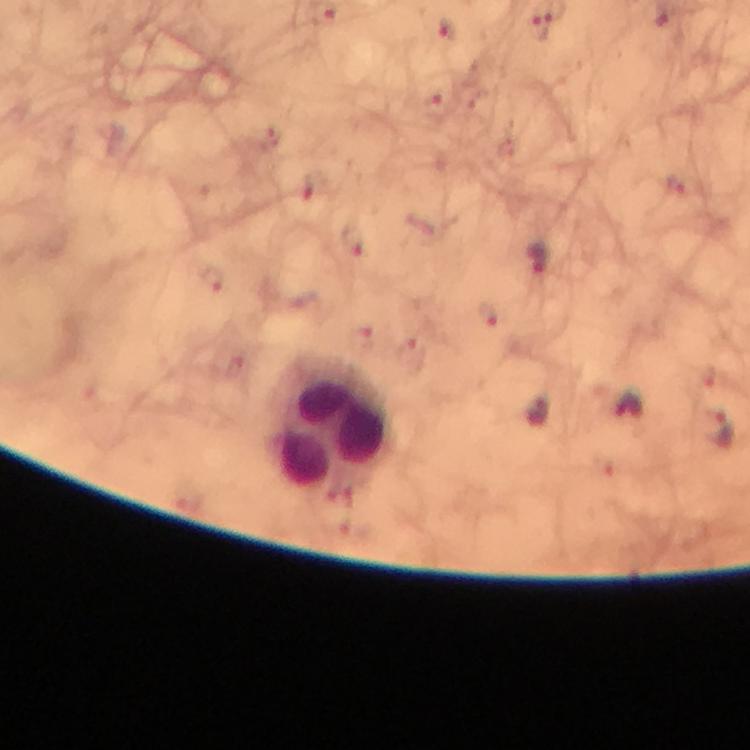
Approximate centers as {x, y} in pixels.
Summary:
  - Plasmodium parasite locations: {447, 28}, {351, 237}, {539, 258}, {719, 429}
  - Leukocyte locations: {331, 425}
  - Context: from a diagnostic examination for malaria
  - Magnification: 100x
  - Image size: 750×750 pixels
  - Capture: smartphone mounted on the microscope
  - Cropped from: one field of view
  - Immersion oil: applied
  - Stain: Giemsa
  - Preparation: thick smear